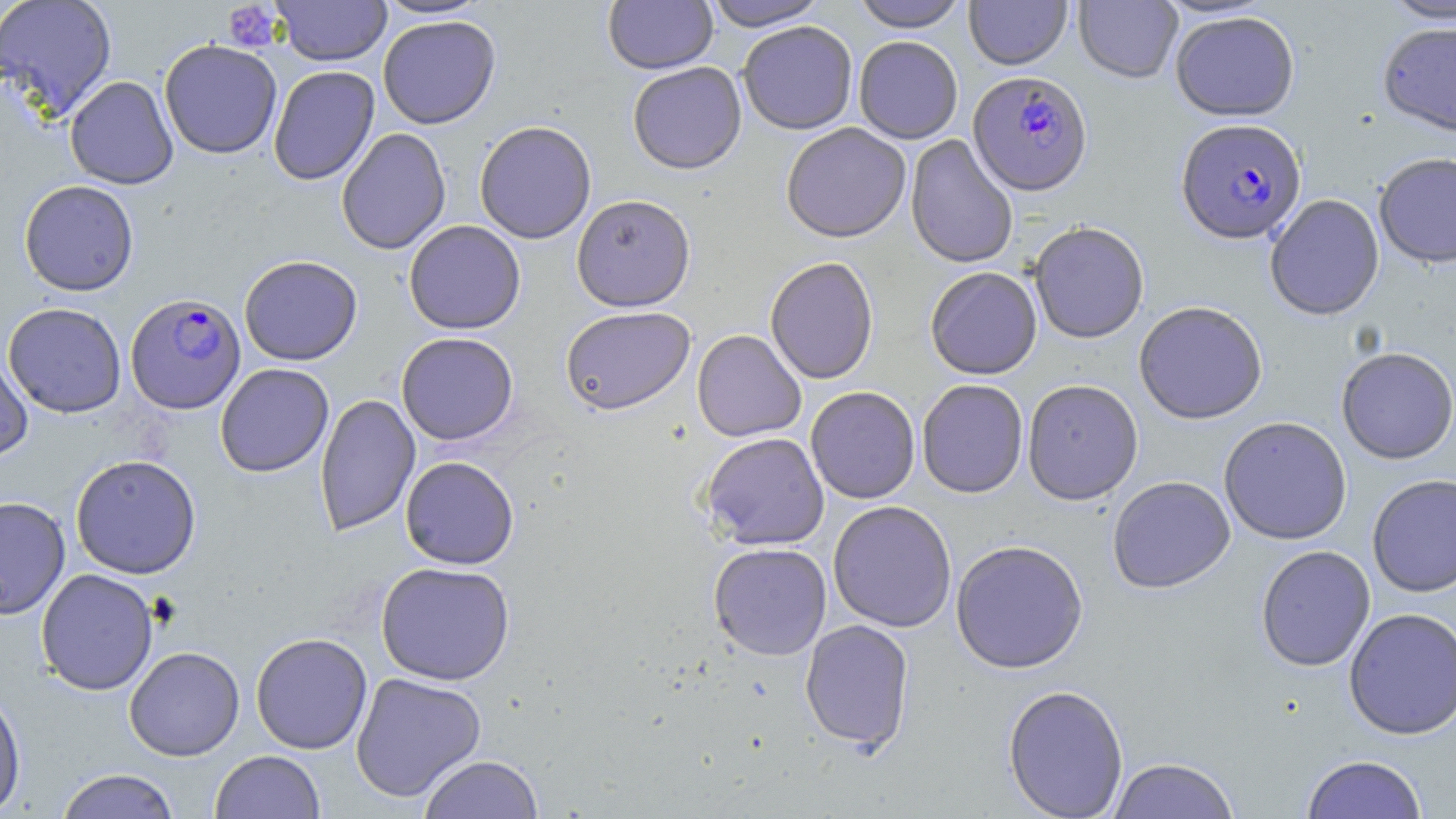

Approximate bounding boxes as (x1, y1, x2, y2) in pixels. Platelet locations: (222, 2, 284, 52). Plasmodium falciparum-infected red blood cell locations: (968, 71, 1093, 196), (1175, 119, 1307, 246), (126, 293, 246, 414). Uninfected red blood cell locations: (0, 0, 117, 120), (271, 0, 392, 66), (374, 0, 490, 19), (603, 0, 718, 74), (703, 0, 828, 31), (850, 0, 968, 32), (964, 0, 1072, 70), (1074, 0, 1182, 84), (1380, 0, 1456, 26), (1170, 11, 1300, 122), (378, 15, 500, 129), (737, 21, 858, 135), (1377, 23, 1456, 140), (853, 36, 963, 144), (159, 39, 282, 159), (627, 61, 747, 174), (268, 65, 380, 186), (64, 75, 178, 189), (474, 120, 597, 244), (781, 123, 911, 243), (336, 128, 451, 255), (905, 134, 1018, 270), (1374, 153, 1456, 271), (19, 179, 139, 296), (571, 194, 695, 312), (1264, 195, 1384, 322), (404, 220, 526, 334), (1028, 222, 1149, 345), (239, 255, 363, 366), (765, 256, 879, 385), (925, 267, 1042, 380), (3, 302, 126, 417), (1133, 303, 1267, 426), (560, 306, 695, 415), (692, 329, 807, 442), (396, 332, 519, 445), (0, 348, 34, 462), (1336, 349, 1456, 466), (215, 363, 334, 477), (917, 379, 1028, 498), (1022, 380, 1143, 506), (805, 386, 920, 504), (314, 393, 420, 536), (1218, 417, 1352, 546), (699, 432, 830, 550), (70, 454, 202, 579), (400, 456, 519, 569), (1367, 475, 1456, 598), (1108, 476, 1236, 594), (0, 496, 71, 619), (828, 501, 957, 632), (950, 539, 1088, 674), (708, 543, 832, 660), (1256, 546, 1376, 672), (375, 561, 516, 685), (36, 568, 159, 695), (1343, 608, 1456, 740), (799, 619, 914, 753), (250, 632, 373, 754), (124, 646, 245, 761), (350, 672, 486, 803), (1002, 684, 1129, 819), (0, 687, 27, 816), (210, 750, 325, 819), (419, 755, 543, 818), (1301, 755, 1428, 818), (1108, 757, 1239, 819), (55, 768, 180, 819). Slide-level diagnosis: Plasmodium falciparum. Thin blood film. Image is 1456×819 pixels. May-Grünwald-Giemsa stain. One field of a larger specimen. Light microscopy. Captured at 1000x magnification.